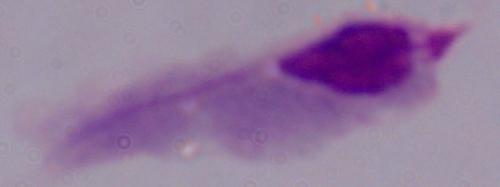

Micrograph. A trichomonad is seen. Captured at 1000x magnification.